Locate every blood parasite and identify its species.
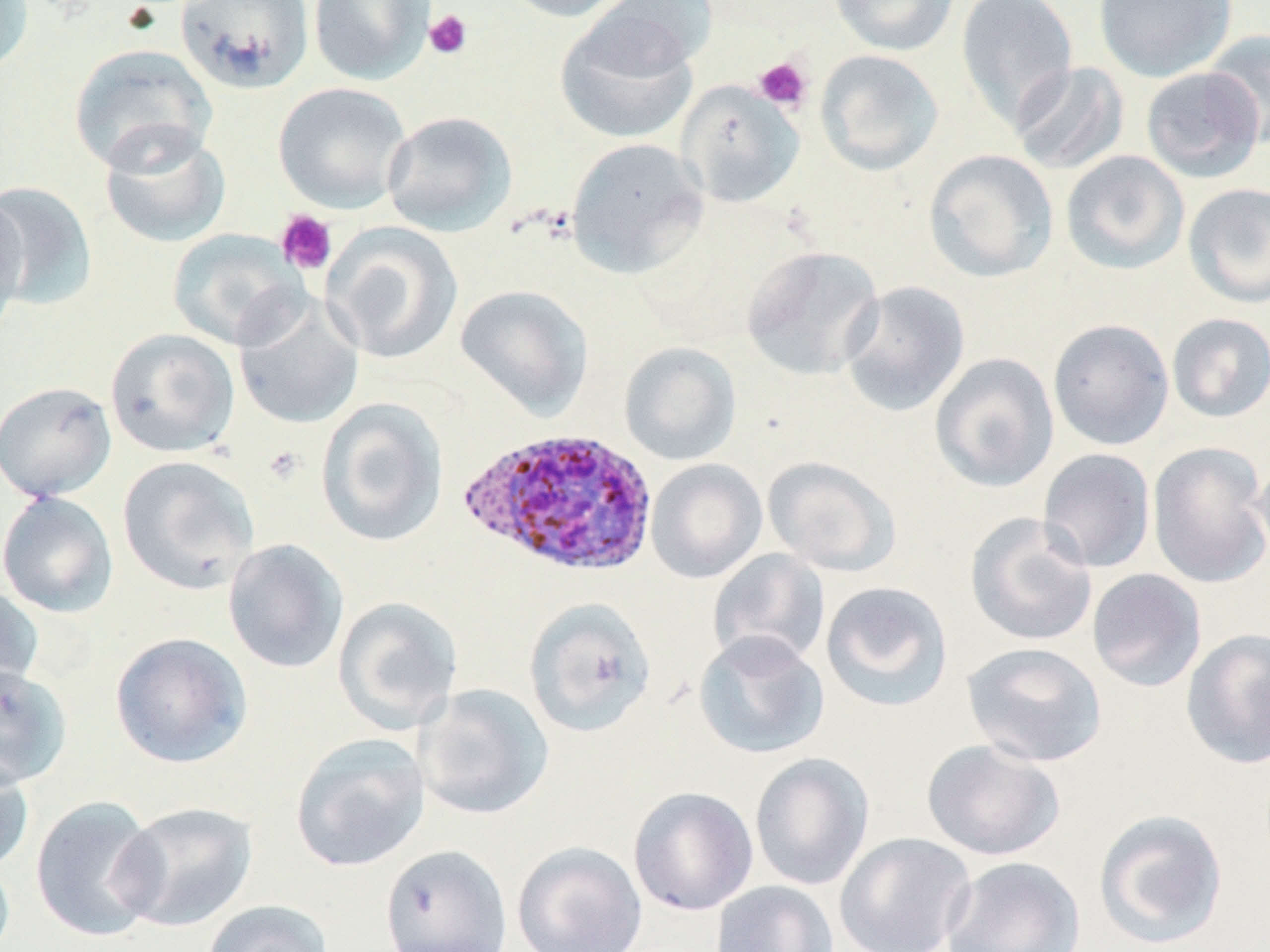

Approximate bounding boxes as [x1, y1, x2, y2] in pixels.
Plasmodium ovale-infected red blood cells: [457, 426, 659, 578].
No Plasmodium falciparum, Plasmodium malariae, Plasmodium vivax, Babesia divergens, or Trypanosoma brucei observed.

Uninfected red blood cell locations: [0, 0, 34, 76], [308, 0, 435, 85], [497, 0, 635, 22], [590, 0, 718, 76], [828, 0, 960, 56], [955, 0, 1078, 130], [1094, 0, 1236, 83], [175, 1, 314, 94], [555, 14, 699, 145], [1203, 29, 1270, 150], [68, 43, 217, 174], [814, 49, 944, 176], [1010, 60, 1130, 176], [1141, 66, 1265, 183], [676, 80, 804, 208], [272, 82, 412, 214], [381, 111, 518, 237], [99, 125, 232, 249], [565, 137, 708, 278], [923, 149, 1059, 283], [1060, 150, 1190, 275], [0, 181, 99, 310], [1182, 182, 1270, 309], [0, 192, 30, 338], [322, 222, 463, 365], [168, 229, 306, 351], [741, 245, 884, 380], [839, 281, 970, 417], [454, 284, 593, 421], [233, 293, 365, 430], [1167, 313, 1270, 423], [1048, 319, 1174, 450], [105, 327, 240, 458], [619, 341, 741, 466], [930, 353, 1059, 493], [0, 381, 116, 501], [315, 397, 449, 548], [1147, 441, 1270, 589], [1038, 448, 1156, 573], [1252, 454, 1270, 571], [117, 455, 260, 595], [763, 456, 902, 577], [646, 459, 767, 584], [0, 491, 118, 618], [965, 512, 1098, 647], [223, 538, 349, 674], [708, 549, 829, 670], [1087, 568, 1207, 692], [0, 580, 44, 703], [820, 580, 954, 712], [332, 595, 464, 734], [523, 597, 658, 738], [1180, 627, 1270, 769], [693, 630, 829, 759], [110, 631, 253, 769], [962, 641, 1108, 767], [0, 664, 72, 789], [414, 684, 554, 820], [290, 732, 430, 873], [921, 738, 1065, 861], [750, 752, 875, 891], [0, 754, 34, 875], [628, 786, 758, 916], [30, 795, 165, 942], [115, 801, 258, 932], [1093, 808, 1230, 949], [834, 832, 977, 952], [511, 841, 647, 952], [378, 844, 513, 952], [0, 853, 15, 952], [940, 854, 1085, 951], [710, 880, 839, 952], [201, 900, 334, 952]. Platelet locations: [424, 9, 473, 60], [753, 56, 813, 112], [275, 209, 338, 275], [262, 445, 306, 486]. Slide-level diagnosis: Plasmodium ovale. Thin blood film. May-Grünwald-Giemsa-stained preparation. Single field of view. Captured at 1000x magnification. Image is 1270×952 pixels. Optical microscopy.